Assess this cell for malaria.
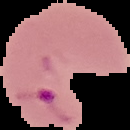

Parasitized.

image size = 130×130 pixels
preparation = thin blood film
image type = segmented cell region on a black background